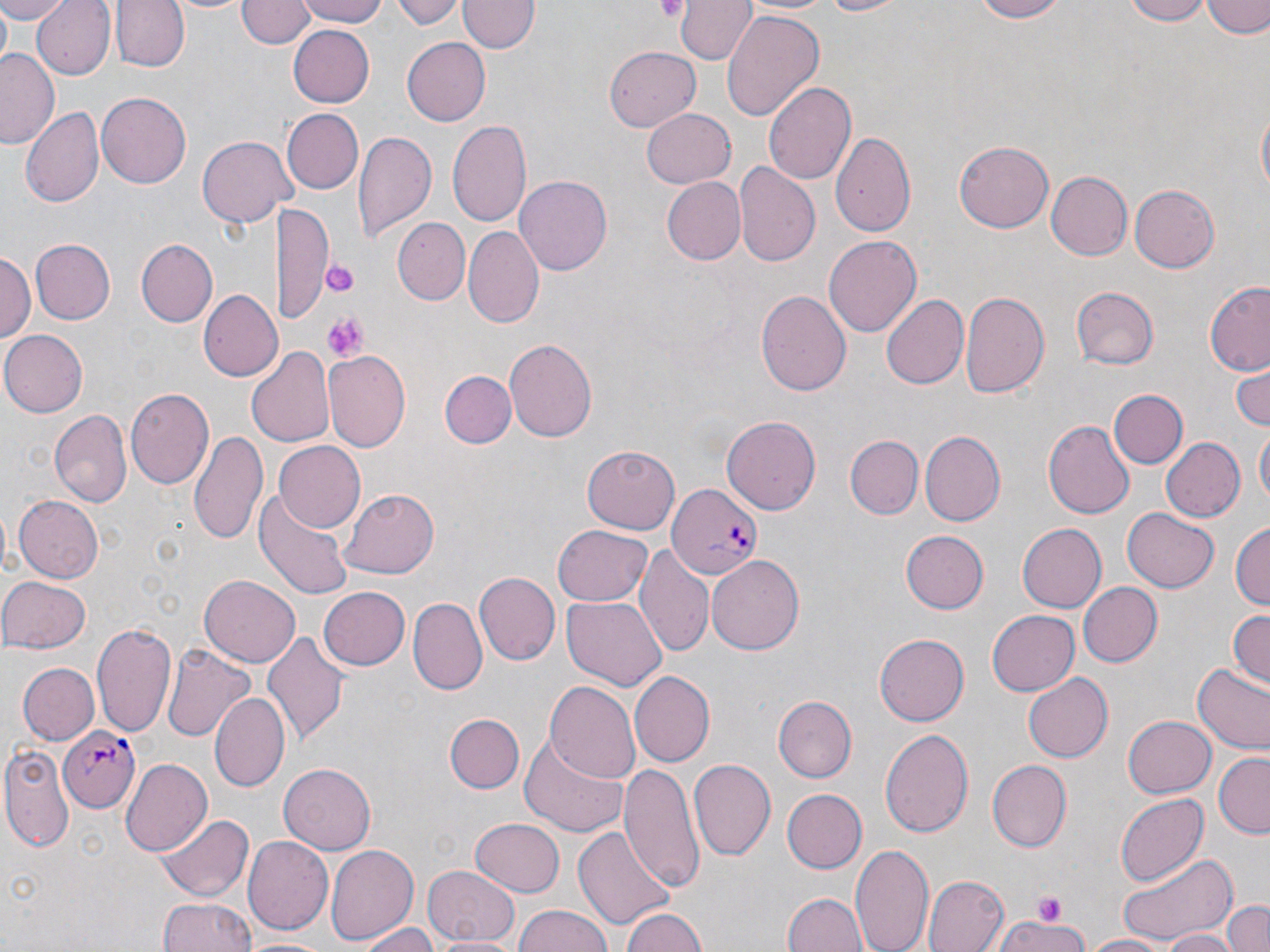
{
  "plasmodium_falciparum_infected_red_blood_cell_locations": "approximate bounding boxes as named x1/y1/x2/y2 corners in pixels: (x1=666, y1=481, x2=762, y2=577), (x1=60, y1=728, x2=141, y2=812)",
  "slide_level_diagnosis": "Plasmodium falciparum",
  "platelet_locations": "approximate bounding boxes as named x1/y1/x2/y2 corners in pixels: (x1=652, y1=0, x2=687, y2=23), (x1=321, y1=255, x2=358, y2=300), (x1=323, y1=311, x2=367, y2=361), (x1=1031, y1=892, x2=1071, y2=923)",
  "modality": "optical microscopy",
  "preparation": "thin blood smear",
  "uninfected_red_blood_cell_locations": "approximate bounding boxes as named x1/y1/x2/y2 corners in pixels: (x1=0, y1=0, x2=69, y2=23), (x1=30, y1=0, x2=114, y2=79), (x1=111, y1=0, x2=189, y2=72), (x1=166, y1=0, x2=255, y2=16), (x1=293, y1=0, x2=393, y2=25), (x1=389, y1=0, x2=464, y2=27), (x1=812, y1=0, x2=915, y2=17), (x1=969, y1=0, x2=1066, y2=24), (x1=1121, y1=0, x2=1216, y2=25), (x1=1203, y1=0, x2=1269, y2=37), (x1=237, y1=1, x2=315, y2=50), (x1=459, y1=1, x2=539, y2=55), (x1=678, y1=1, x2=754, y2=64), (x1=722, y1=11, x2=823, y2=119), (x1=288, y1=28, x2=373, y2=108), (x1=404, y1=39, x2=490, y2=125), (x1=603, y1=45, x2=701, y2=130), (x1=1, y1=47, x2=61, y2=148), (x1=763, y1=80, x2=858, y2=186), (x1=96, y1=92, x2=192, y2=187), (x1=1255, y1=102, x2=1269, y2=206), (x1=642, y1=106, x2=736, y2=186), (x1=21, y1=107, x2=104, y2=208), (x1=282, y1=108, x2=363, y2=193), (x1=447, y1=118, x2=531, y2=228), (x1=354, y1=128, x2=435, y2=241), (x1=831, y1=131, x2=917, y2=239), (x1=199, y1=134, x2=289, y2=228), (x1=955, y1=140, x2=1055, y2=233), (x1=735, y1=163, x2=821, y2=268), (x1=1044, y1=171, x2=1132, y2=261), (x1=516, y1=176, x2=612, y2=274), (x1=660, y1=176, x2=746, y2=264), (x1=1128, y1=182, x2=1220, y2=274), (x1=278, y1=204, x2=334, y2=324), (x1=395, y1=217, x2=470, y2=304), (x1=463, y1=227, x2=543, y2=330), (x1=824, y1=234, x2=924, y2=337), (x1=28, y1=238, x2=115, y2=324), (x1=136, y1=239, x2=217, y2=326), (x1=2, y1=249, x2=33, y2=349), (x1=1203, y1=281, x2=1270, y2=376), (x1=1071, y1=286, x2=1158, y2=369), (x1=199, y1=289, x2=281, y2=382), (x1=755, y1=290, x2=850, y2=399), (x1=960, y1=291, x2=1049, y2=401), (x1=880, y1=294, x2=969, y2=390), (x1=0, y1=328, x2=87, y2=419), (x1=503, y1=337, x2=597, y2=444), (x1=248, y1=344, x2=335, y2=448), (x1=324, y1=349, x2=411, y2=450), (x1=1231, y1=358, x2=1269, y2=431), (x1=441, y1=370, x2=516, y2=448), (x1=125, y1=388, x2=212, y2=491), (x1=1108, y1=389, x2=1188, y2=468), (x1=49, y1=409, x2=131, y2=509), (x1=722, y1=415, x2=821, y2=514), (x1=1043, y1=421, x2=1134, y2=521), (x1=1254, y1=426, x2=1270, y2=505), (x1=189, y1=428, x2=268, y2=547), (x1=921, y1=432, x2=1005, y2=525), (x1=844, y1=435, x2=922, y2=519), (x1=1161, y1=438, x2=1246, y2=522), (x1=273, y1=441, x2=366, y2=532), (x1=581, y1=444, x2=680, y2=535), (x1=339, y1=488, x2=438, y2=579), (x1=254, y1=489, x2=354, y2=598), (x1=13, y1=495, x2=102, y2=584), (x1=1122, y1=507, x2=1219, y2=592), (x1=1231, y1=521, x2=1269, y2=614), (x1=1016, y1=523, x2=1105, y2=612), (x1=550, y1=525, x2=653, y2=607), (x1=900, y1=530, x2=988, y2=615), (x1=635, y1=544, x2=715, y2=659), (x1=706, y1=552, x2=804, y2=652), (x1=472, y1=570, x2=559, y2=663), (x1=199, y1=572, x2=300, y2=665), (x1=0, y1=575, x2=91, y2=653), (x1=410, y1=582, x2=551, y2=679), (x1=1077, y1=582, x2=1161, y2=667), (x1=318, y1=586, x2=410, y2=671), (x1=562, y1=595, x2=666, y2=690), (x1=411, y1=597, x2=485, y2=693), (x1=1226, y1=608, x2=1270, y2=688), (x1=986, y1=610, x2=1081, y2=695), (x1=91, y1=618, x2=178, y2=739), (x1=263, y1=631, x2=347, y2=745), (x1=875, y1=632, x2=970, y2=726), (x1=164, y1=642, x2=255, y2=744), (x1=1193, y1=662, x2=1270, y2=755), (x1=17, y1=663, x2=98, y2=744), (x1=1024, y1=671, x2=1113, y2=763), (x1=629, y1=673, x2=714, y2=767), (x1=546, y1=682, x2=641, y2=782), (x1=210, y1=692, x2=289, y2=794), (x1=774, y1=696, x2=856, y2=781), (x1=445, y1=712, x2=523, y2=793), (x1=1122, y1=715, x2=1216, y2=799), (x1=881, y1=727, x2=975, y2=836), (x1=518, y1=732, x2=631, y2=838), (x1=3, y1=742, x2=74, y2=852), (x1=1214, y1=753, x2=1269, y2=837), (x1=121, y1=758, x2=212, y2=857), (x1=689, y1=758, x2=775, y2=860), (x1=986, y1=760, x2=1069, y2=851), (x1=620, y1=763, x2=704, y2=895), (x1=279, y1=764, x2=374, y2=854), (x1=780, y1=787, x2=866, y2=873), (x1=1114, y1=792, x2=1210, y2=885), (x1=156, y1=812, x2=253, y2=902), (x1=471, y1=817, x2=564, y2=896), (x1=576, y1=823, x2=675, y2=930), (x1=243, y1=836, x2=332, y2=934), (x1=851, y1=841, x2=934, y2=952), (x1=325, y1=842, x2=421, y2=945), (x1=1115, y1=849, x2=1237, y2=946), (x1=422, y1=866, x2=520, y2=946), (x1=923, y1=874, x2=1009, y2=952), (x1=784, y1=893, x2=864, y2=952), (x1=157, y1=897, x2=256, y2=952), (x1=1223, y1=899, x2=1270, y2=952), (x1=621, y1=905, x2=709, y2=952), (x1=514, y1=907, x2=614, y2=952), (x1=994, y1=915, x2=1089, y2=952), (x1=357, y1=921, x2=440, y2=952), (x1=1156, y1=929, x2=1245, y2=952), (x1=429, y1=934, x2=521, y2=952), (x1=243, y1=935, x2=333, y2=952), (x1=1084, y1=935, x2=1169, y2=952)",
  "stain": "May-Grünwald-Giemsa",
  "image_size": "1270×952 pixels",
  "magnification": "1000x",
  "field_of_view": "single"
}